Look for Plasmodium parasites.
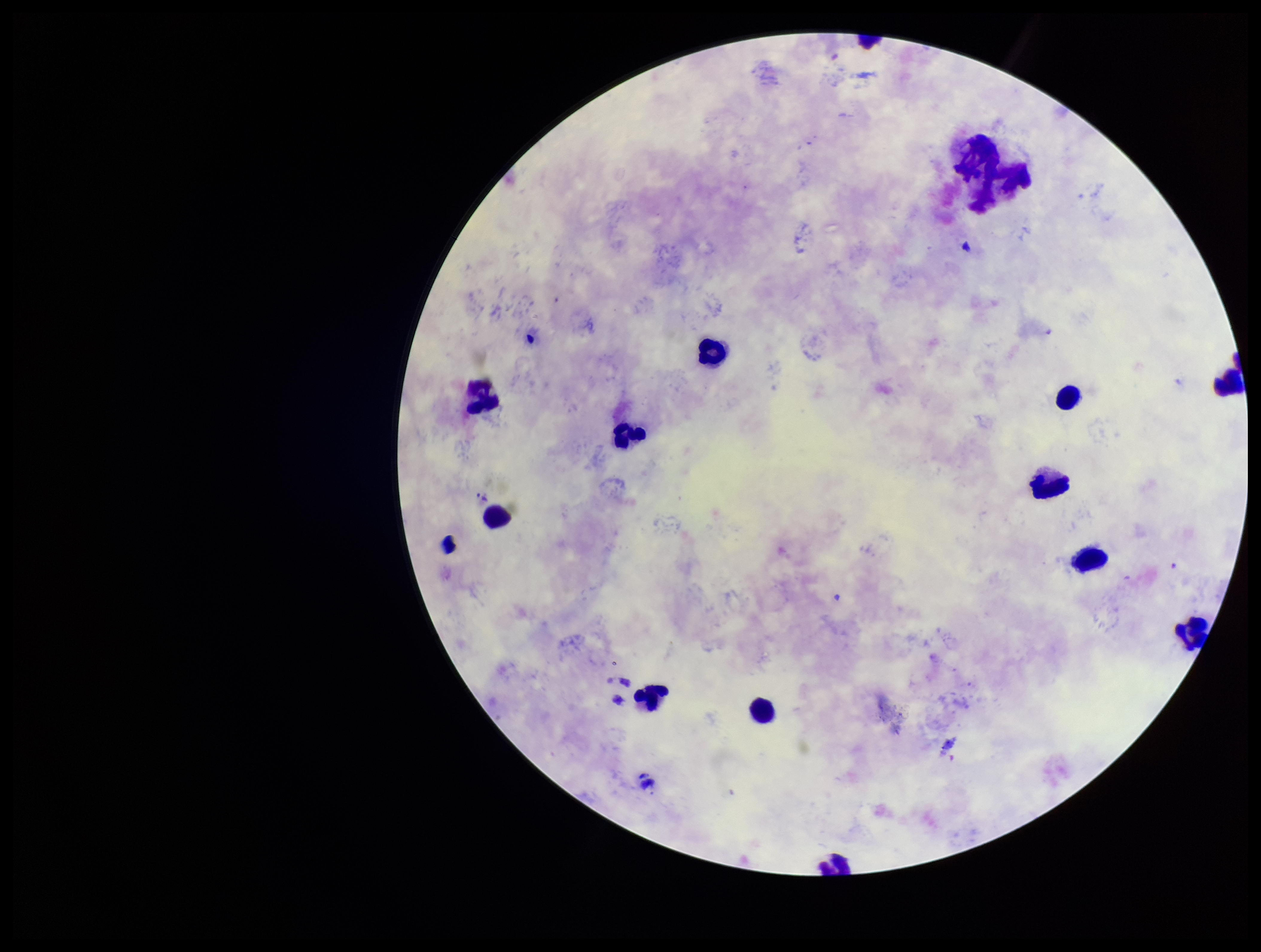

None detected.

stain = Giemsa
image size = 1261×952 pixels
species reported for this patient = Plasmodium vivax
leukocyte count = 13
field of view = one from this slide
preparation = thick blood smear
parasite count = 0
patient malaria status = infected
capture = smartphone photograph through the microscope eyepiece